Name the blood parasite species.
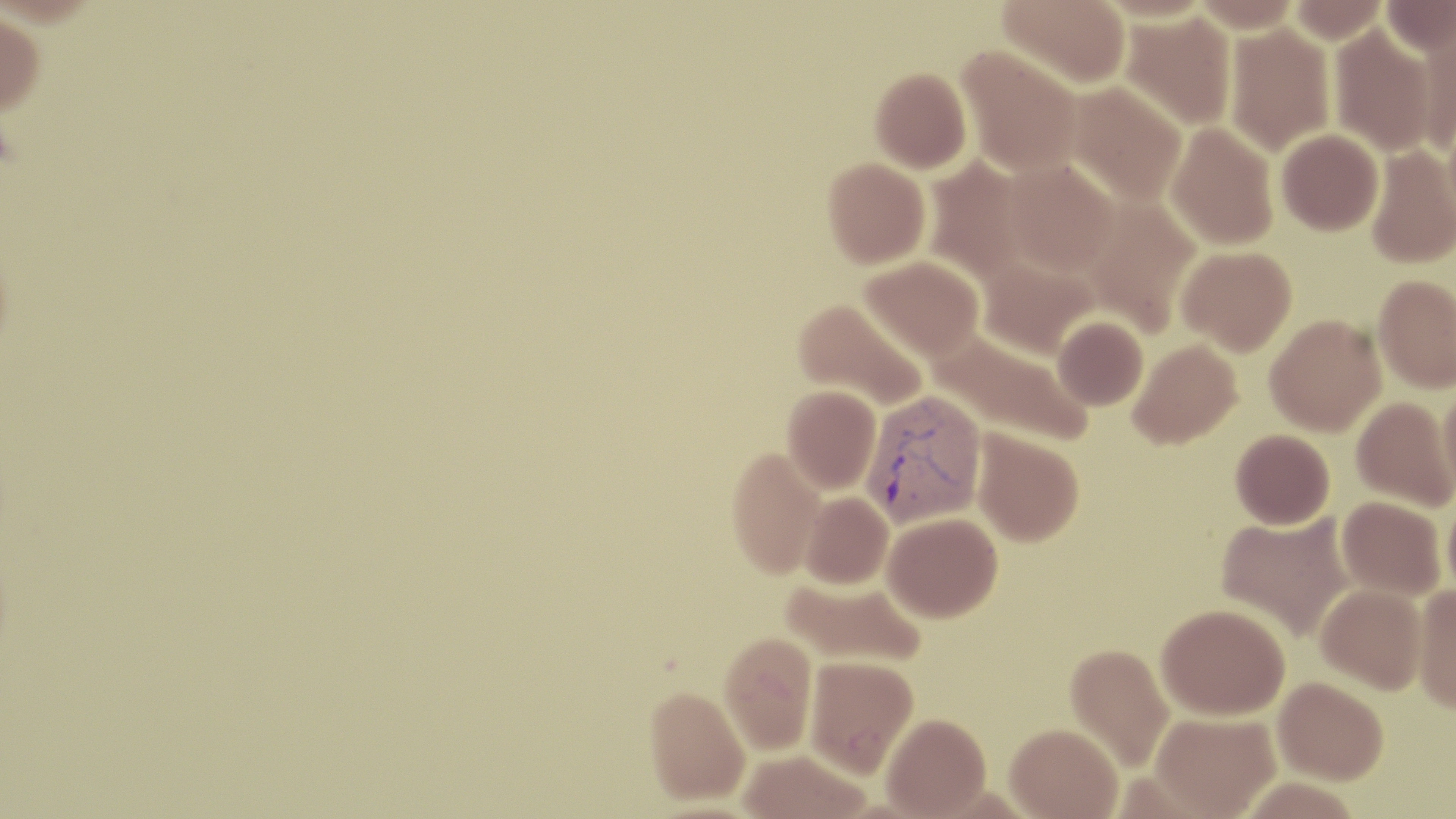

Plasmodium vivax.

Summary:
  - Coordinate format: approximate bounding boxes as [x1, y1, x2, y2] in pixels
  - Uninfected red blood cell locations: [997, 0, 1130, 89], [1190, 0, 1303, 33], [1288, 0, 1389, 44], [1381, 0, 1456, 57], [0, 11, 45, 116], [1118, 11, 1237, 131], [1414, 19, 1456, 154], [1223, 23, 1335, 157], [1328, 23, 1438, 156], [955, 45, 1085, 178], [870, 67, 972, 173], [1062, 81, 1188, 207], [1165, 122, 1279, 251], [1276, 129, 1383, 235], [1365, 143, 1456, 269], [821, 157, 931, 268], [922, 157, 1029, 285], [1001, 159, 1121, 277], [1082, 195, 1203, 337], [1176, 245, 1298, 356], [860, 255, 984, 361], [975, 255, 1099, 361], [1373, 274, 1456, 392], [792, 298, 928, 412], [1264, 314, 1386, 436], [1051, 315, 1149, 411], [926, 327, 1094, 449], [1127, 339, 1243, 449], [1438, 382, 1456, 503], [783, 386, 881, 494], [1351, 397, 1455, 511], [971, 428, 1084, 547], [1230, 429, 1335, 529], [726, 445, 826, 580], [1442, 488, 1456, 608], [799, 491, 893, 589], [1336, 496, 1446, 600], [882, 512, 1003, 622], [1215, 512, 1356, 642], [781, 576, 927, 668], [1316, 584, 1427, 694], [1412, 584, 1456, 716], [1157, 603, 1290, 719], [718, 631, 818, 754], [1064, 642, 1174, 772], [804, 655, 919, 777], [1273, 676, 1389, 785], [643, 685, 751, 804], [1149, 711, 1280, 818], [882, 712, 991, 818], [1005, 723, 1123, 818], [737, 750, 870, 819]
  - Plasmodium vivax-infected red blood cell locations: [860, 389, 988, 528]
  - Modality: optical microscopy
  - Preparation: thin blood film
  - Field of view: one of a larger specimen
  - Image size: 1456×819 pixels
  - Stain: May-Grünwald-Giemsa
  - Magnification: 1000x